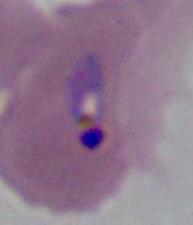 A Plasmodium parasite is shown. Captured at either 400x or 1000x magnification. Micrograph.